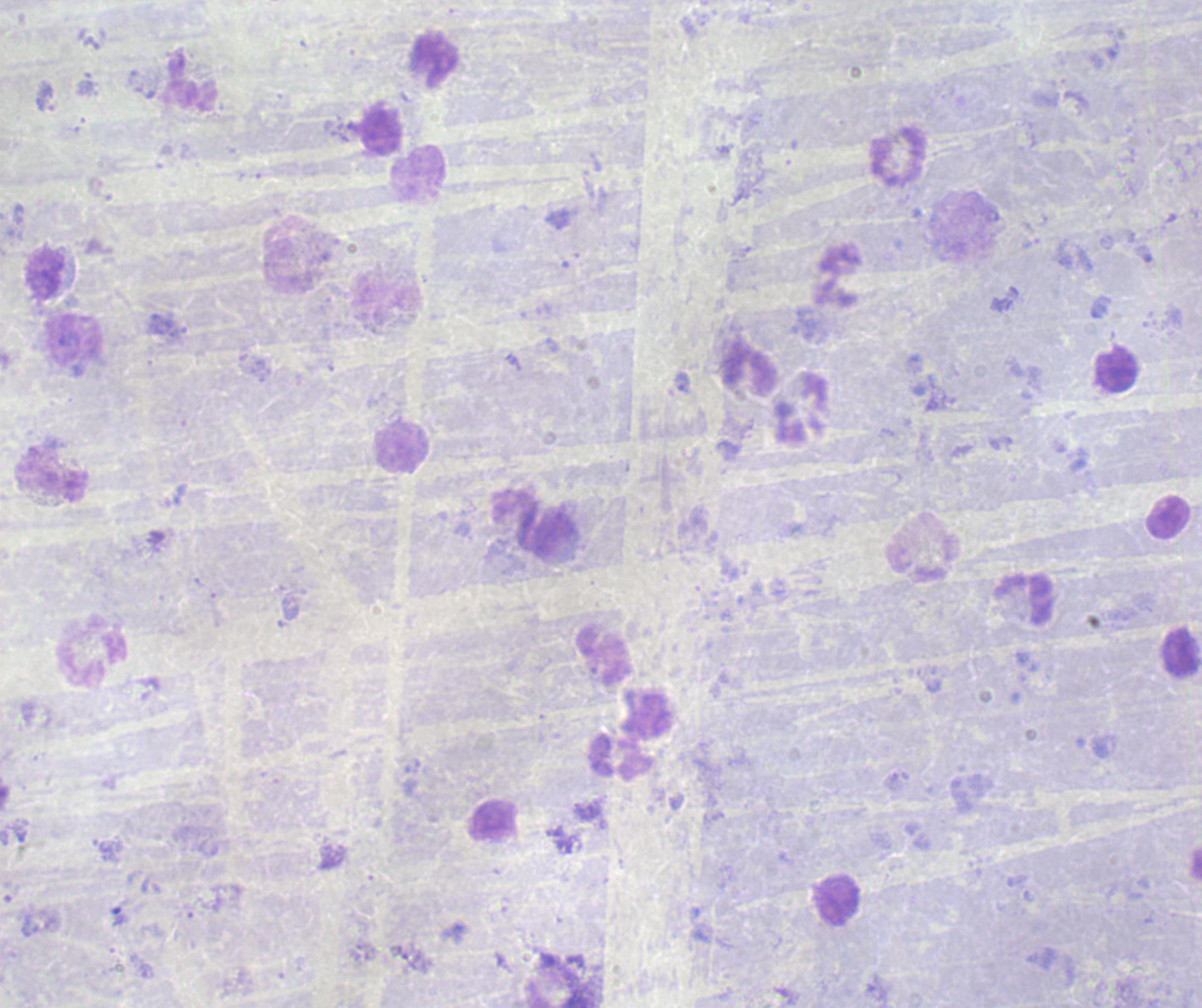

Approximate object centers, in pixels from the top-left corner.
Summary:
  - Trophozoite locations: (x=682, y=383)
  - Leukocyte locations: (x=900, y=157), (x=417, y=172), (x=45, y=275), (x=1116, y=369), (x=749, y=371), (x=53, y=475), (x=534, y=523), (x=1023, y=600), (x=91, y=654), (x=605, y=656), (x=620, y=756), (x=838, y=900)
  - Image size: 1202×1008 pixels
  - Background quality: unsatisfactory
  - Field of view: single
  - Magnification: 100x
  - Preparation: thick smear of blood
  - Context: previously used in an actual diagnosis
  - Result: Plasmodium parasites detected
  - Stain: Romanowsky